Outline each blood parasite and name the species.
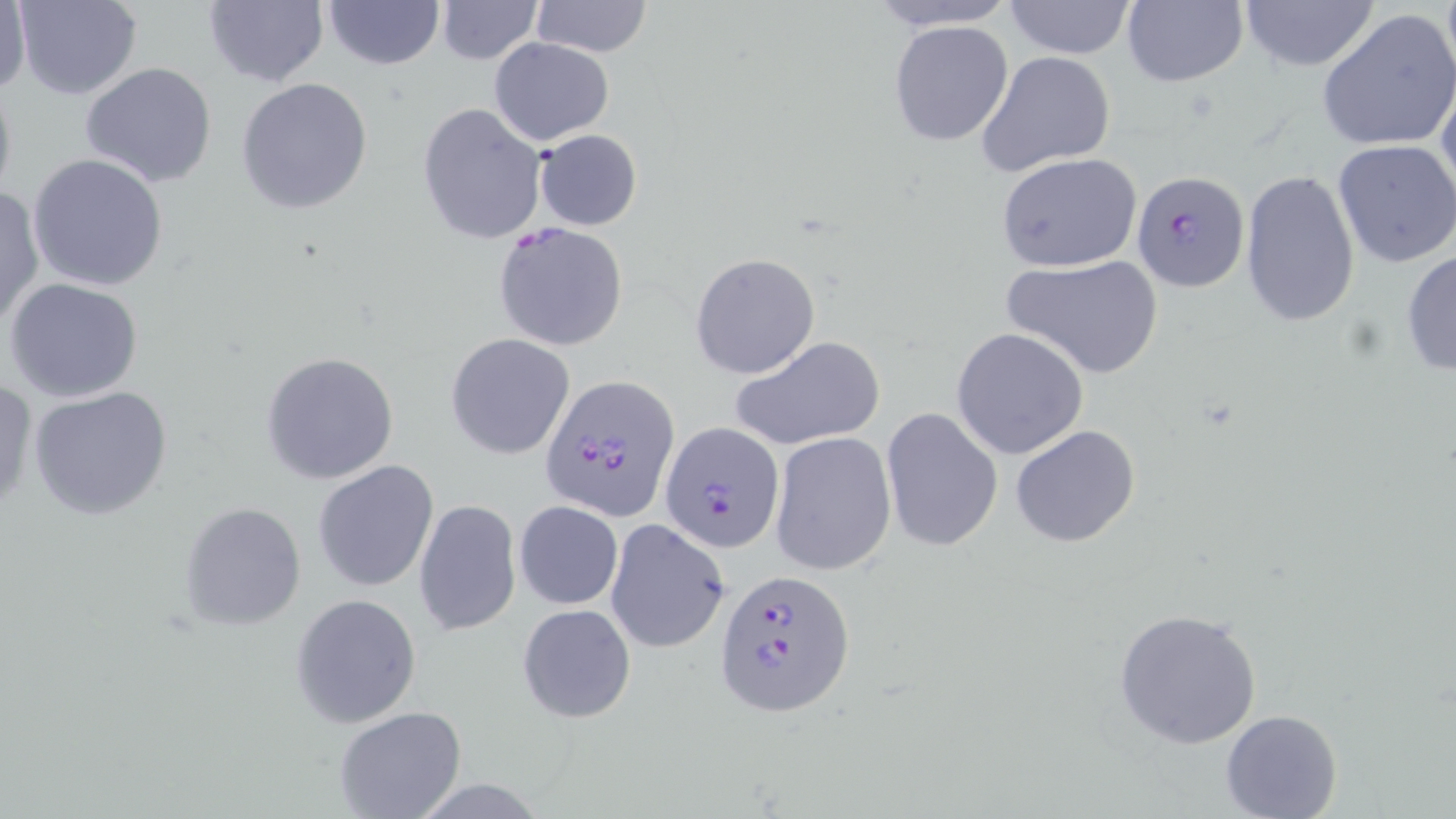
Approximate bounding boxes as (x1, y1, x2, y2) in pixels.
Plasmodium falciparum-infected red blood cells: (1131, 171, 1249, 292), (540, 375, 679, 522), (661, 422, 785, 554), (716, 569, 854, 716).
No Plasmodium ovale, Plasmodium malariae, Plasmodium vivax, Babesia divergens, or Trypanosoma brucei observed.

Uninfected red blood cell locations: (15, 0, 143, 100), (322, 0, 444, 70), (435, 0, 541, 65), (531, 0, 652, 59), (868, 0, 1016, 31), (1002, 0, 1139, 59), (1236, 0, 1381, 71), (2, 1, 31, 101), (203, 1, 328, 87), (1120, 1, 1249, 88), (1317, 8, 1456, 154), (888, 19, 1014, 147), (488, 37, 615, 146), (977, 51, 1117, 178), (79, 61, 220, 188), (1435, 67, 1456, 205), (0, 70, 17, 209), (236, 76, 374, 215), (417, 102, 547, 244), (533, 128, 642, 230), (1332, 139, 1456, 269), (995, 152, 1142, 272), (29, 153, 169, 292), (1238, 170, 1361, 329), (0, 187, 44, 330), (492, 222, 629, 353), (1401, 248, 1456, 379), (689, 252, 820, 379), (1002, 254, 1163, 380), (4, 276, 144, 403), (951, 328, 1089, 459), (446, 333, 576, 460), (730, 335, 885, 451), (260, 350, 402, 486), (0, 376, 37, 515), (28, 384, 173, 522), (880, 406, 1003, 554), (1010, 424, 1141, 547), (769, 431, 897, 576), (312, 459, 439, 592), (414, 500, 520, 637), (513, 501, 623, 609), (178, 502, 307, 631), (604, 519, 729, 653), (290, 594, 422, 728), (517, 602, 636, 723), (1112, 607, 1262, 749), (333, 707, 468, 819), (1221, 708, 1343, 818). Slide-level diagnosis: Plasmodium falciparum. May-Grünwald-Giemsa stain. 1000x magnification. Image is 1456×819 pixels. Single field of view. Thin blood smear. Light microscopy.